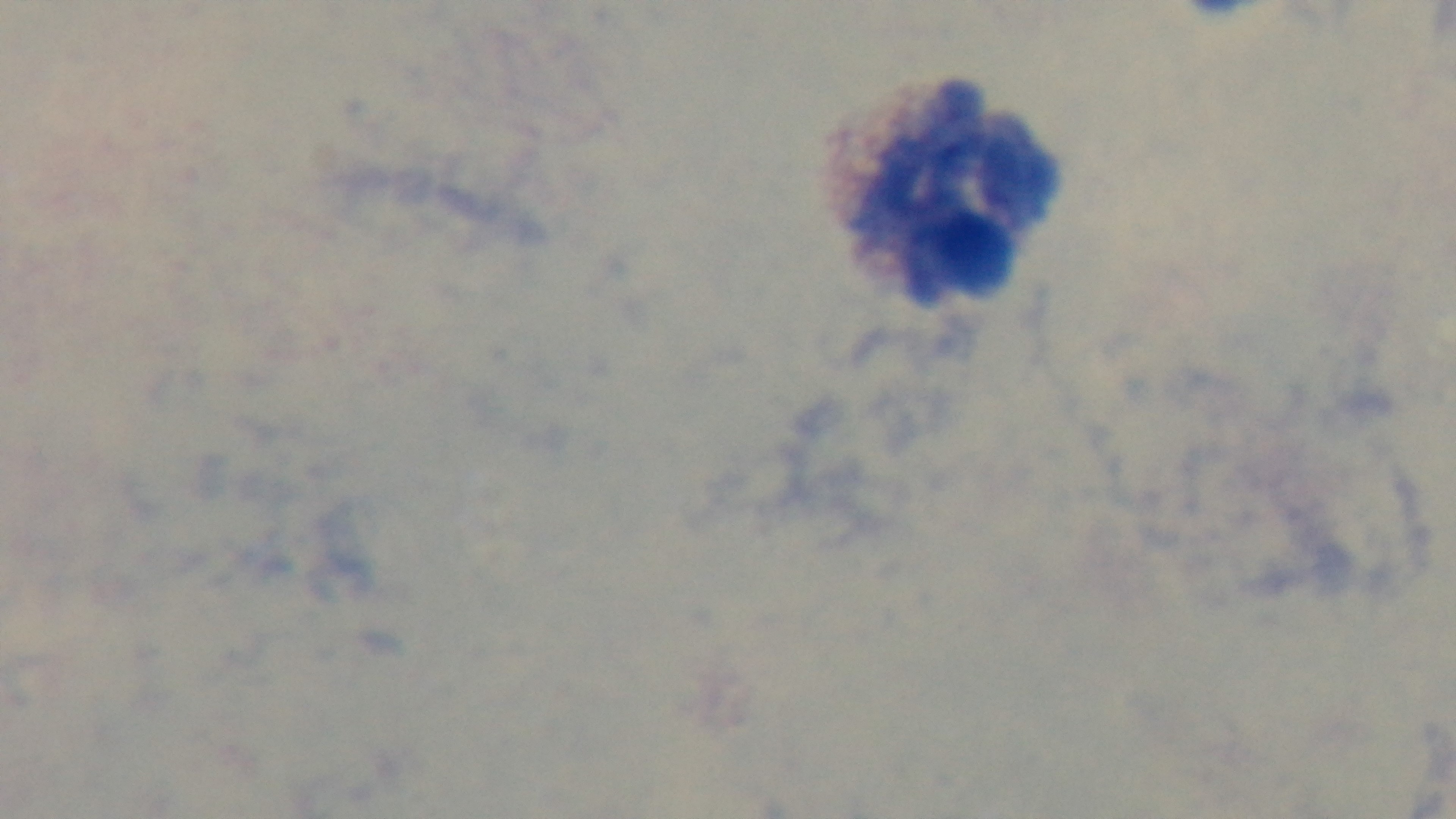 Single field of view. Giemsa-stained. Preparation: thick. Captured with a mounted 4K digital camera. Malaria status: uninfected. Oil-immersion objective, 100x. Light microscopy.